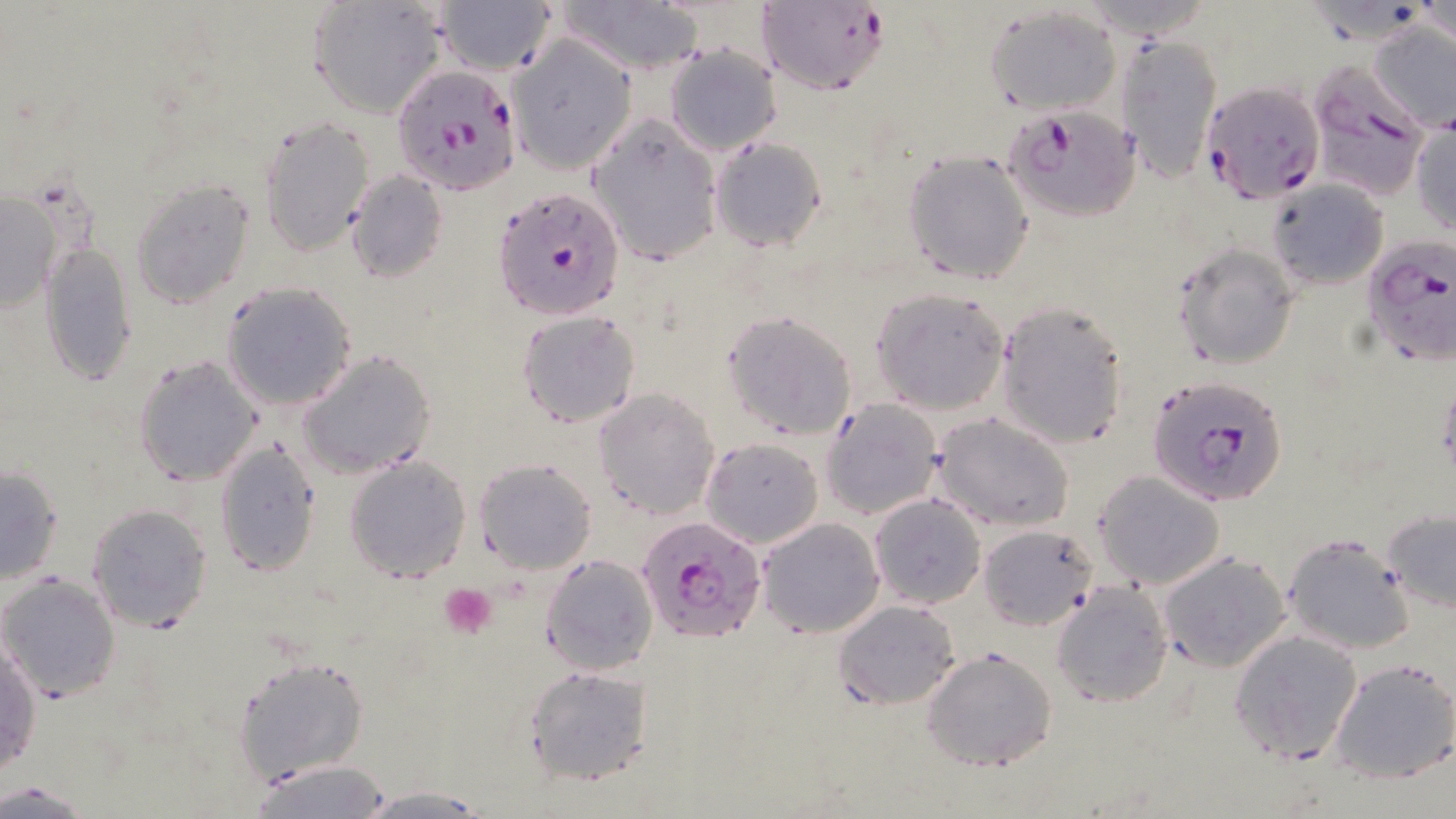
{
  "slide_level_diagnosis": "Plasmodium falciparum",
  "field_of_view": "one of a larger specimen",
  "image_size": "1456×819 pixels",
  "preparation": "thin blood smear",
  "uninfected_red_blood_cell_locations": "approximate bounding boxes as named x1/y1/x2/y2 corners in pixels: (x1=305, y1=0, x2=446, y2=118), (x1=557, y1=0, x2=707, y2=73), (x1=436, y1=1, x2=556, y2=77), (x1=1418, y1=1, x2=1456, y2=54), (x1=987, y1=7, x2=1121, y2=114), (x1=1367, y1=21, x2=1456, y2=132), (x1=1117, y1=34, x2=1223, y2=183), (x1=507, y1=37, x2=636, y2=173), (x1=664, y1=44, x2=780, y2=156), (x1=588, y1=114, x2=724, y2=266), (x1=259, y1=116, x2=374, y2=255), (x1=1410, y1=117, x2=1456, y2=236), (x1=710, y1=136, x2=828, y2=252), (x1=903, y1=150, x2=1035, y2=285), (x1=346, y1=170, x2=446, y2=283), (x1=131, y1=179, x2=255, y2=308), (x1=1267, y1=181, x2=1388, y2=290), (x1=1, y1=186, x2=63, y2=317), (x1=1172, y1=244, x2=1299, y2=369), (x1=40, y1=245, x2=136, y2=387), (x1=222, y1=283, x2=356, y2=411), (x1=870, y1=288, x2=1009, y2=415), (x1=995, y1=302, x2=1130, y2=448), (x1=516, y1=310, x2=641, y2=429), (x1=722, y1=310, x2=858, y2=442), (x1=297, y1=350, x2=435, y2=479), (x1=134, y1=353, x2=262, y2=487), (x1=593, y1=387, x2=720, y2=520), (x1=823, y1=398, x2=943, y2=519), (x1=932, y1=415, x2=1074, y2=532), (x1=700, y1=437, x2=823, y2=549), (x1=215, y1=442, x2=321, y2=575), (x1=345, y1=455, x2=471, y2=583), (x1=476, y1=458, x2=597, y2=574), (x1=0, y1=466, x2=64, y2=585), (x1=1092, y1=472, x2=1224, y2=590), (x1=868, y1=493, x2=988, y2=609), (x1=86, y1=503, x2=213, y2=633), (x1=1381, y1=508, x2=1456, y2=614), (x1=756, y1=517, x2=885, y2=640), (x1=980, y1=522, x2=1096, y2=631), (x1=1281, y1=532, x2=1416, y2=654), (x1=1157, y1=551, x2=1293, y2=674), (x1=541, y1=554, x2=659, y2=675), (x1=1, y1=573, x2=120, y2=702), (x1=1050, y1=584, x2=1172, y2=709), (x1=832, y1=599, x2=960, y2=708), (x1=1229, y1=629, x2=1364, y2=763), (x1=1, y1=640, x2=41, y2=775), (x1=920, y1=646, x2=1060, y2=772), (x1=234, y1=655, x2=370, y2=787), (x1=1330, y1=658, x2=1456, y2=785), (x1=523, y1=664, x2=655, y2=786), (x1=246, y1=759, x2=396, y2=818), (x1=0, y1=779, x2=92, y2=816), (x1=356, y1=787, x2=491, y2=817)",
  "stain": "May-Grünwald-Giemsa",
  "magnification": "1000x",
  "plasmodium_falciparum_infected_red_blood_cell_locations": "approximate bounding boxes as named x1/y1/x2/y2 corners in pixels: (x1=756, y1=0, x2=891, y2=95), (x1=392, y1=64, x2=522, y2=196), (x1=1307, y1=67, x2=1429, y2=201), (x1=1200, y1=81, x2=1322, y2=206), (x1=1005, y1=106, x2=1139, y2=223), (x1=492, y1=185, x2=625, y2=321), (x1=1361, y1=236, x2=1456, y2=368), (x1=1147, y1=374, x2=1289, y2=509), (x1=637, y1=517, x2=765, y2=644)",
  "modality": "optical microscopy",
  "platelet_locations": "approximate bounding boxes as named x1/y1/x2/y2 corners in pixels: (x1=441, y1=584, x2=498, y2=640)"
}